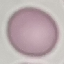
Summary:
  - Malaria status: uninfected
  - Stain: Giemsa
  - Capture: smartphone through the microscope eyepiece
  - Image type: automatically extracted cell patch, resized to 64 × 64 pixels
  - Preparation: thin smear